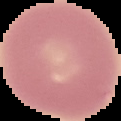
image type = segmented cell region on a black background
malaria status = uninfected
image size = 121×121 pixels
preparation = thin blood film